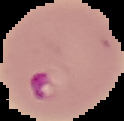
Result: Plasmodium parasites detected. From a thin blood smear. Cell region segmented out of the field of view; the surrounding area is masked to black. Image is 124×121 pixels.